Assess this cell for malaria.
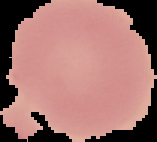
Uninfected.

{
  "image_type": "segmented cell region with the area outside set to black",
  "image_size": "157×142 pixels",
  "preparation": "thin blood smear"
}